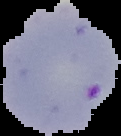

From a thin blood smear. Malaria status: parasitized. Image is 121×136 pixels. Segmented cell region on a black background.